Comment on the morphology of the erythrocytes.
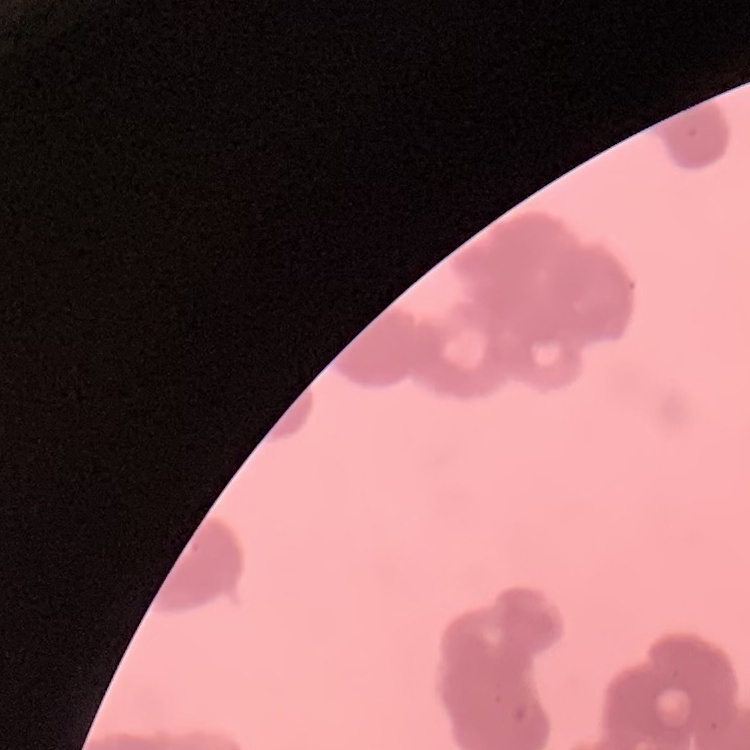
Rouleaux formation.

Summary:
  - Preparation: thin blood film
  - Image type: square crop of a larger photomicrograph
  - Stain: Field's or Giemsa